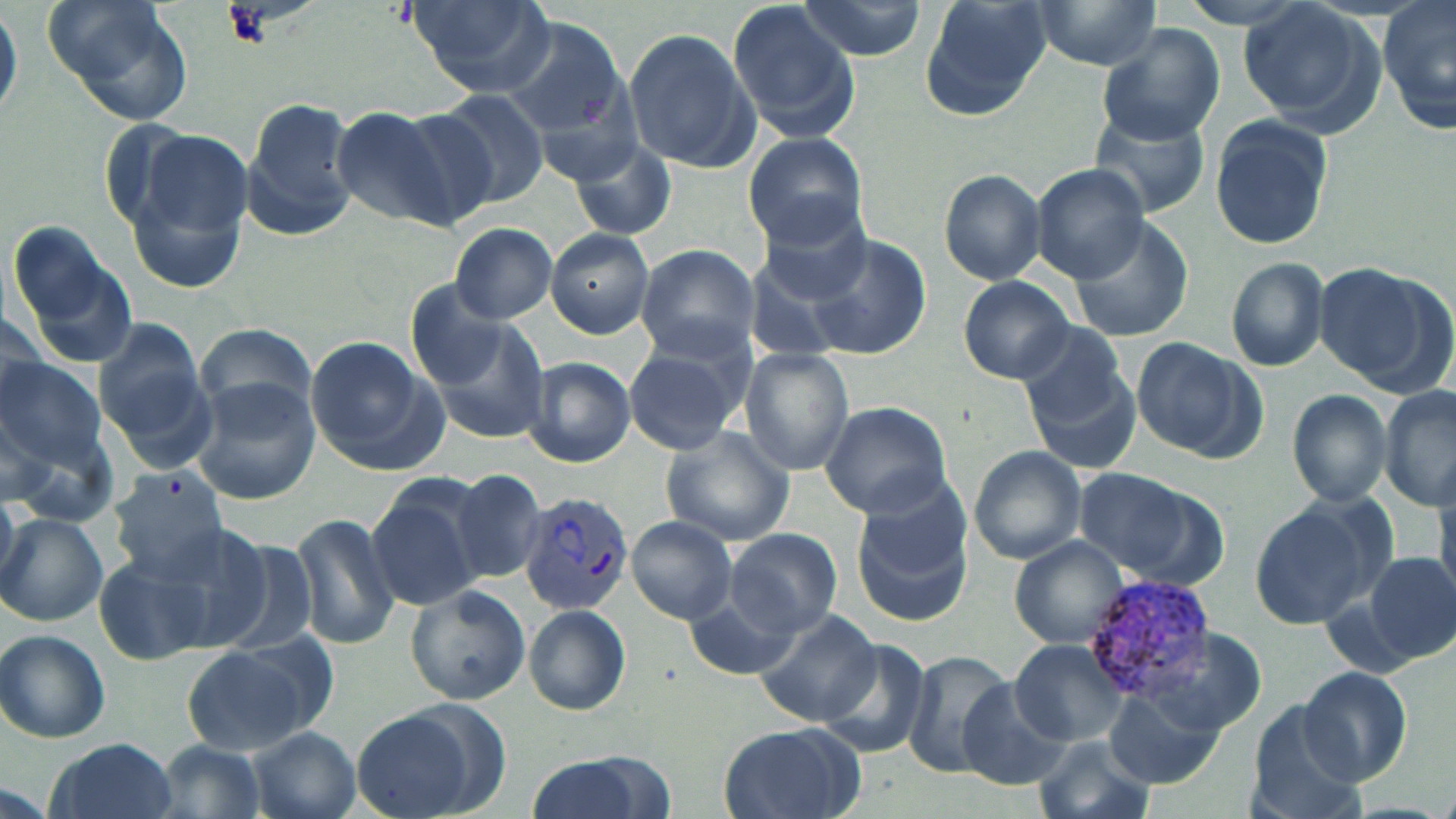
{
  "slide_level_diagnosis": "Plasmodium vivax",
  "field_of_view": "single",
  "plasmodium_vivax_infected_red_blood_cell_locations": "approximate bounding boxes as named x1/y1/x2/y2 corners in pixels: (x1=519, y1=490, x2=634, y2=615), (x1=1083, y1=573, x2=1218, y2=697)",
  "uninfected_red_blood_cell_locations": "approximate bounding boxes as named x1/y1/x2/y2 corners in pixels: (x1=40, y1=0, x2=196, y2=129), (x1=410, y1=0, x2=554, y2=95), (x1=794, y1=0, x2=928, y2=59), (x1=918, y1=0, x2=1052, y2=115), (x1=1030, y1=0, x2=1170, y2=70), (x1=1180, y1=0, x2=1314, y2=32), (x1=1379, y1=0, x2=1455, y2=135), (x1=728, y1=1, x2=861, y2=139), (x1=1237, y1=1, x2=1382, y2=131), (x1=0, y1=2, x2=21, y2=124), (x1=501, y1=17, x2=632, y2=147), (x1=623, y1=26, x2=759, y2=173), (x1=1098, y1=26, x2=1224, y2=145), (x1=429, y1=92, x2=549, y2=211), (x1=242, y1=96, x2=360, y2=240), (x1=330, y1=105, x2=461, y2=227), (x1=1088, y1=109, x2=1213, y2=220), (x1=390, y1=110, x2=501, y2=228), (x1=1207, y1=117, x2=1337, y2=251), (x1=125, y1=131, x2=253, y2=288), (x1=742, y1=132, x2=868, y2=251), (x1=568, y1=137, x2=677, y2=240), (x1=1029, y1=162, x2=1151, y2=283), (x1=938, y1=169, x2=1047, y2=284), (x1=754, y1=202, x2=875, y2=305), (x1=1071, y1=216, x2=1195, y2=342), (x1=6, y1=219, x2=141, y2=373), (x1=450, y1=222, x2=557, y2=324), (x1=547, y1=228, x2=654, y2=338), (x1=801, y1=233, x2=930, y2=359), (x1=634, y1=244, x2=760, y2=359), (x1=1226, y1=257, x2=1329, y2=370), (x1=1314, y1=262, x2=1441, y2=388), (x1=957, y1=276, x2=1074, y2=382), (x1=0, y1=310, x2=50, y2=416), (x1=420, y1=311, x2=552, y2=445), (x1=95, y1=317, x2=213, y2=459), (x1=1012, y1=318, x2=1131, y2=425), (x1=194, y1=323, x2=321, y2=419), (x1=304, y1=334, x2=446, y2=473), (x1=622, y1=336, x2=753, y2=456), (x1=1131, y1=336, x2=1264, y2=462), (x1=739, y1=348, x2=854, y2=474), (x1=522, y1=357, x2=636, y2=467), (x1=0, y1=362, x2=108, y2=470), (x1=1026, y1=362, x2=1142, y2=477), (x1=188, y1=380, x2=320, y2=504), (x1=1381, y1=384, x2=1456, y2=510), (x1=1286, y1=389, x2=1392, y2=507), (x1=818, y1=401, x2=952, y2=518), (x1=0, y1=405, x2=57, y2=507), (x1=661, y1=425, x2=797, y2=546), (x1=968, y1=447, x2=1087, y2=564), (x1=1070, y1=466, x2=1220, y2=585), (x1=108, y1=467, x2=230, y2=580), (x1=449, y1=471, x2=545, y2=584), (x1=365, y1=477, x2=485, y2=608), (x1=851, y1=482, x2=978, y2=629), (x1=1250, y1=498, x2=1384, y2=629), (x1=292, y1=511, x2=397, y2=650), (x1=1, y1=512, x2=106, y2=626), (x1=626, y1=516, x2=737, y2=623), (x1=726, y1=528, x2=841, y2=637), (x1=1011, y1=537, x2=1129, y2=648), (x1=213, y1=540, x2=322, y2=655), (x1=97, y1=552, x2=219, y2=665), (x1=1366, y1=553, x2=1455, y2=663), (x1=405, y1=582, x2=530, y2=705), (x1=683, y1=588, x2=807, y2=683), (x1=524, y1=605, x2=630, y2=714), (x1=755, y1=609, x2=884, y2=728), (x1=0, y1=630, x2=111, y2=743), (x1=812, y1=637, x2=933, y2=757), (x1=1011, y1=639, x2=1127, y2=746), (x1=183, y1=641, x2=321, y2=755), (x1=903, y1=649, x2=1013, y2=776), (x1=1298, y1=665, x2=1413, y2=786), (x1=955, y1=678, x2=1070, y2=792), (x1=1104, y1=689, x2=1223, y2=788), (x1=1243, y1=704, x2=1365, y2=819), (x1=350, y1=705, x2=489, y2=819), (x1=718, y1=723, x2=865, y2=819), (x1=249, y1=728, x2=359, y2=819), (x1=1033, y1=737, x2=1156, y2=819), (x1=44, y1=738, x2=180, y2=819), (x1=151, y1=741, x2=271, y2=819), (x1=526, y1=753, x2=656, y2=819)",
  "stain": "May-Grünwald-Giemsa",
  "magnification": "1000x",
  "modality": "light microscopy",
  "preparation": "thin blood smear",
  "image_size": "1456×819 pixels"
}